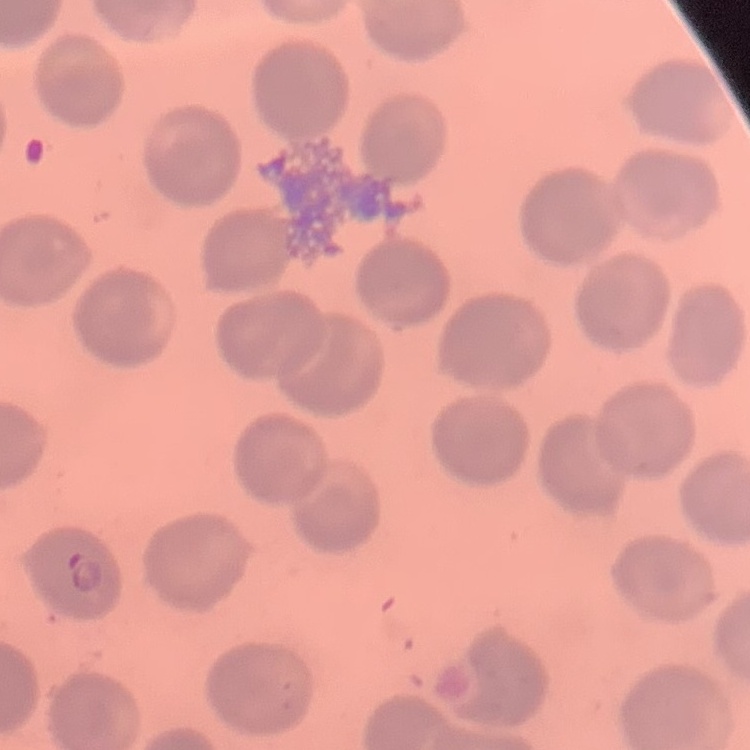 The red blood cells exhibit no rouleaux formation. Stained with either Field's or Giemsa. Square crop of a larger photomicrograph. Thin blood film.